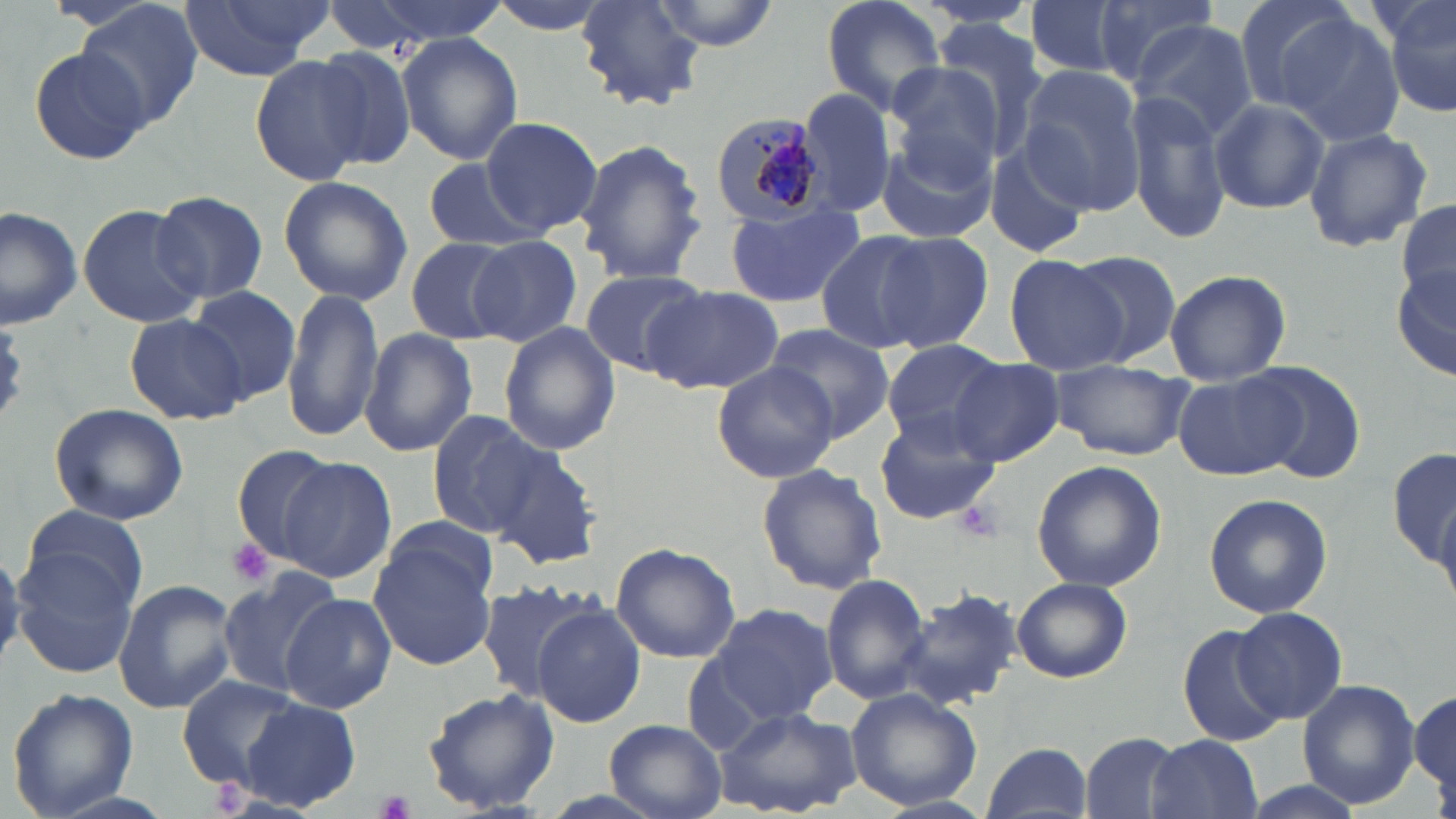

Summary:
  - Coordinate format: approximate bounding boxes as [x1, y1, x2, y2] in pixels
  - Uninfected red blood cell locations: [72, 0, 201, 128], [174, 0, 336, 82], [323, 0, 510, 49], [484, 0, 617, 35], [576, 0, 705, 109], [650, 0, 780, 50], [817, 0, 950, 119], [1023, 0, 1129, 78], [1227, 0, 1359, 111], [1380, 0, 1456, 121], [1089, 1, 1219, 90], [1259, 5, 1404, 140], [926, 19, 1055, 164], [1131, 20, 1258, 141], [398, 32, 523, 166], [26, 45, 153, 167], [310, 45, 422, 169], [251, 53, 374, 185], [884, 66, 1002, 182], [1017, 67, 1146, 213], [797, 87, 900, 218], [1129, 87, 1231, 244], [1207, 95, 1330, 214], [481, 116, 602, 237], [1303, 126, 1432, 252], [874, 134, 996, 244], [985, 136, 1095, 261], [575, 137, 708, 286], [422, 158, 540, 253], [278, 176, 411, 306], [151, 191, 268, 306], [1395, 199, 1456, 307], [724, 201, 865, 309], [77, 203, 204, 329], [0, 205, 82, 329], [815, 231, 933, 354], [874, 231, 995, 354], [467, 235, 583, 347], [405, 237, 517, 346], [1062, 250, 1181, 365], [1005, 253, 1127, 373], [1392, 261, 1456, 384], [575, 267, 710, 373], [1164, 268, 1292, 384], [542, 283, 667, 404], [282, 286, 383, 444], [644, 286, 781, 394], [190, 288, 300, 402], [125, 312, 249, 426], [498, 322, 621, 455], [764, 326, 895, 441], [361, 328, 477, 458], [881, 338, 1003, 447], [711, 359, 840, 483], [948, 359, 1065, 468], [1049, 362, 1191, 458], [1244, 362, 1366, 484], [1172, 372, 1305, 480], [49, 403, 189, 527], [426, 410, 547, 541], [874, 411, 1001, 526], [1389, 443, 1455, 587], [230, 444, 341, 565], [488, 445, 603, 570], [279, 459, 397, 582], [1031, 460, 1168, 592], [756, 463, 887, 596], [1204, 493, 1333, 618], [18, 508, 147, 617], [367, 530, 499, 672], [11, 541, 144, 680], [610, 541, 741, 663], [215, 570, 344, 700], [821, 571, 934, 705], [1011, 577, 1132, 683], [113, 578, 235, 713], [473, 579, 598, 702], [900, 585, 1025, 710], [281, 593, 396, 714], [705, 602, 838, 724], [532, 604, 646, 727], [1231, 607, 1348, 724], [1178, 625, 1288, 747], [176, 675, 306, 791], [1297, 679, 1421, 808], [6, 687, 138, 816], [422, 688, 559, 814], [845, 689, 983, 811], [1410, 690, 1455, 798], [239, 697, 362, 812], [714, 703, 862, 819], [604, 718, 727, 819], [1082, 732, 1186, 819], [1146, 735, 1262, 819], [982, 741, 1091, 819]
  - Plasmodium malariae-infected red blood cell locations: [709, 109, 826, 226]
  - Platelet locations: [952, 501, 1004, 543], [225, 539, 274, 585], [379, 790, 416, 819]
  - Slide-level diagnosis: Plasmodium malariae
  - Preparation: thin blood smear
  - Stain: May-Grünwald-Giemsa
  - Image size: 1456×819 pixels
  - Magnification: 1000x
  - Field of view: single
  - Modality: light microscopy